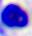
Summary:
  - Magnification: 400x
  - Identification: white blood cell
  - Modality: photomicrograph